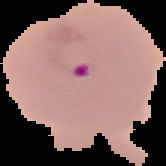

Malaria status: parasitized. Image is 166×166 pixels. The area outside the segmented cell region is set to black. From a thin blood smear.